Identify the cell.
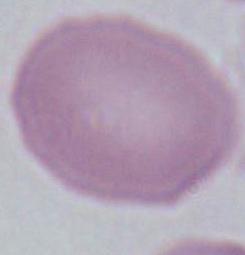

This is an erythrocyte.

Summary:
  - Magnification: 1000x
  - Modality: micrograph